Assess this cell for malaria.
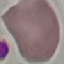

Uninfected.

Summary:
  - Image type: automatically extracted cell patch, resized to 64 × 64 pixels
  - Stain: Giemsa
  - Capture: smartphone camera at the microscope eyepiece
  - Preparation: thin smear